Classify this cell by malaria status.
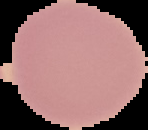
It is uninfected.

{
  "preparation": "thin blood smear",
  "image_size": "148×130 pixels",
  "image_type": "cell region segmented out of the field of view; surrounding area masked to black"
}